Classify this cell by malaria status.
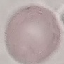
Uninfected.

Acquired by smartphone through the microscope eyepiece. Cell patch, automatically extracted from a larger field of view and resized to 64 × 64 pixels. Thin smear of blood. Giemsa-stained preparation.